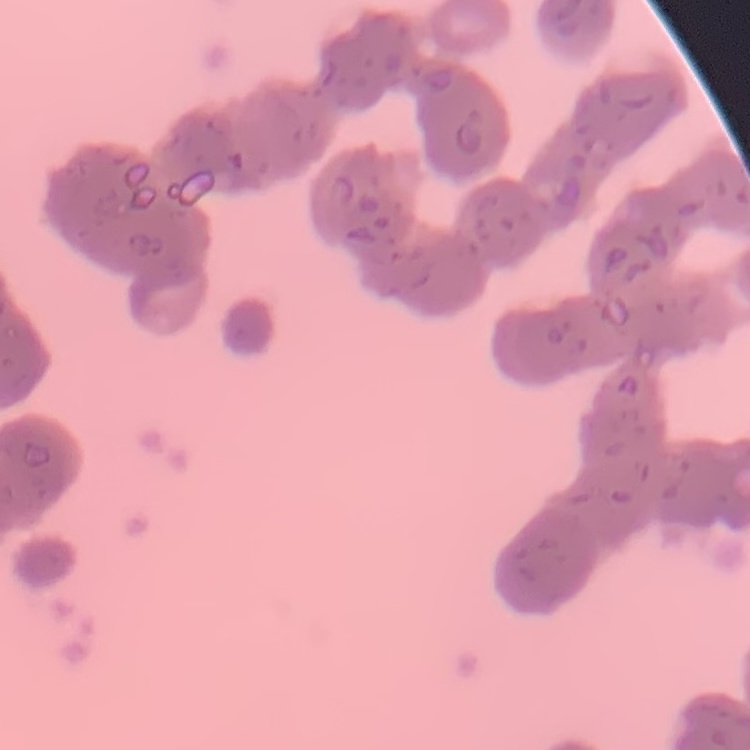

{
  "erythrocyte_morphology": "rouleaux formation",
  "stain": "Field's or Giemsa",
  "preparation": "thin peripheral smear",
  "image_type": "square crop of a larger photomicrograph"
}